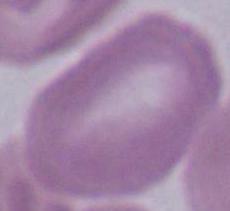
Summary:
  - Identification: erythrocyte
  - Modality: photomicrograph
  - Magnification: 1000x